Assess this cell for malaria.
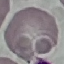

It is uninfected.

preparation = thin blood film
capture = smartphone camera at the microscope eyepiece
image type = cell patch, automatically extracted from a larger field of view and resized to 64 × 64 pixels
stain = Giemsa